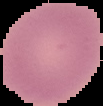
Segmented cell region on a black background. Malaria status: uninfected. From a thin blood film. Image is 103×106 pixels.